Report the malaria status of this cell.
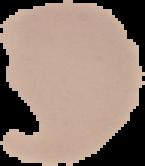

It is uninfected.

{
  "preparation": "thin blood smear",
  "image_size": "145×166 pixels",
  "image_type": "segmented cell region with the area outside set to black"
}